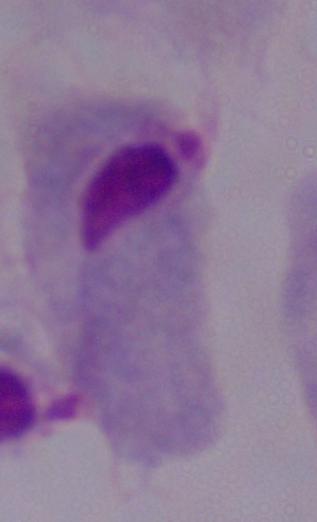
modality = photomicrograph
identification = trichomonad
magnification = 1000x